Classify this cell by malaria status.
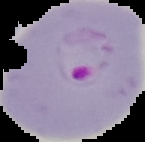
It is parasitized.

image type = segmented cell region on a black background
preparation = thin blood smear
image size = 145×142 pixels